State which cell type is depicted.
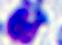
This is a leukocyte.

modality: micrograph
magnification: 400x